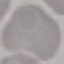

malaria status = uninfected
image type = cell patch, automatically extracted from a larger field of view and resized to 64 × 64 pixels
stain = Giemsa
capture = smartphone through the microscope eyepiece
preparation = thin blood film